State which parasite is depicted.
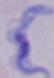
A trypanosome.

1000x magnification. Micrograph.